Name the parasite shown.
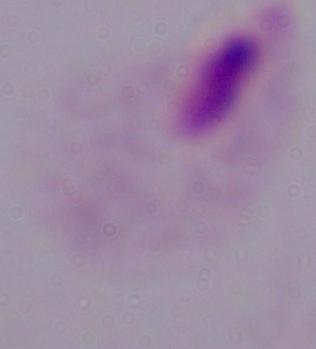
This is a trichomonad.

1000x magnification. Micrograph.